Assess the morphology of the red blood cells.
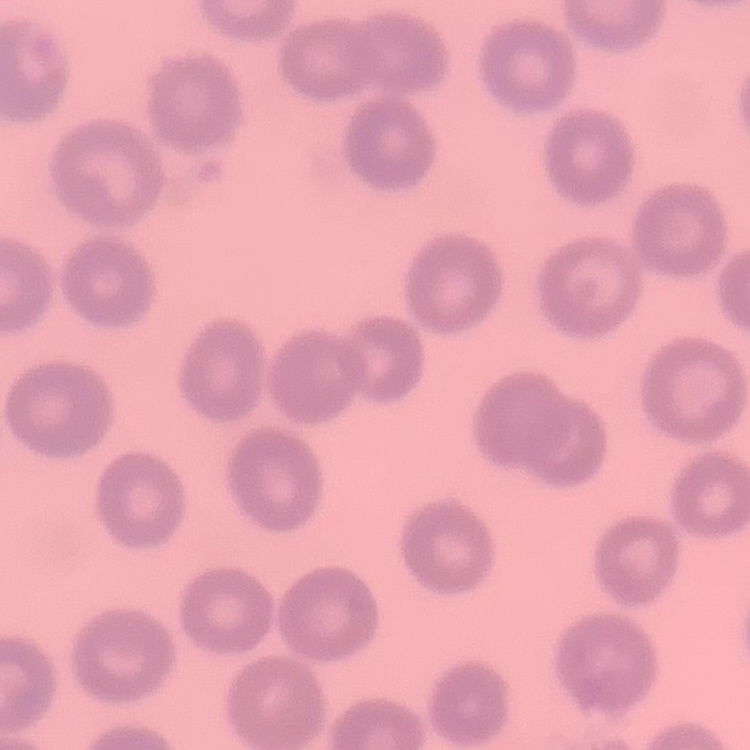

No rouleaux formation.

Thin blood smear. Square crop of a larger photomicrograph. Stained with either Field's or Giemsa.